Report the malaria status of this cell.
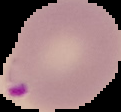

It is parasitized.

Summary:
  - Image type: cell region segmented out of the field of view; surrounding area masked to black
  - Preparation: thin blood film
  - Image size: 121×112 pixels